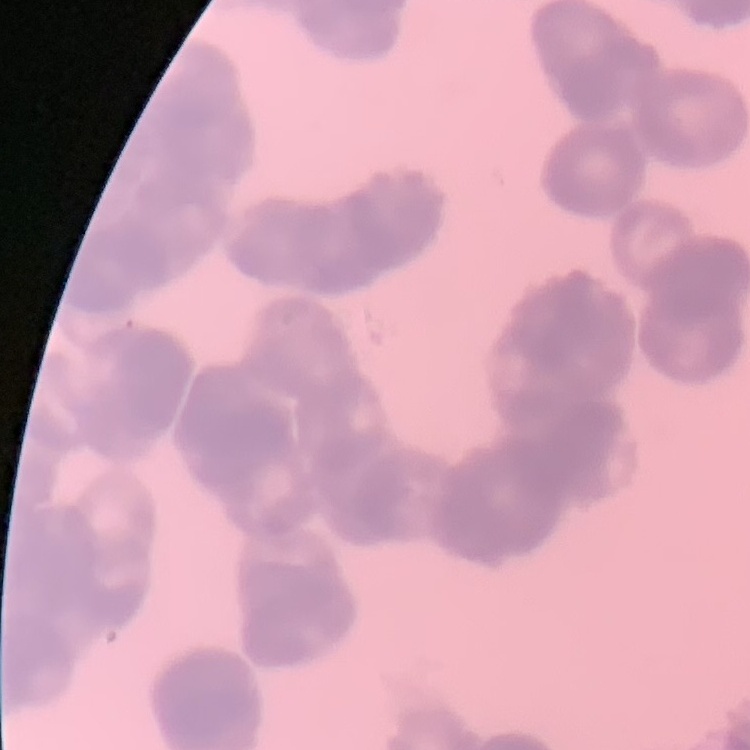
The red blood cells exhibit rouleaux formation. One tile cut from a larger photomicrograph. Stained with either Field's or Giemsa. Thin blood film.